Assess the morphology of the red blood cells.
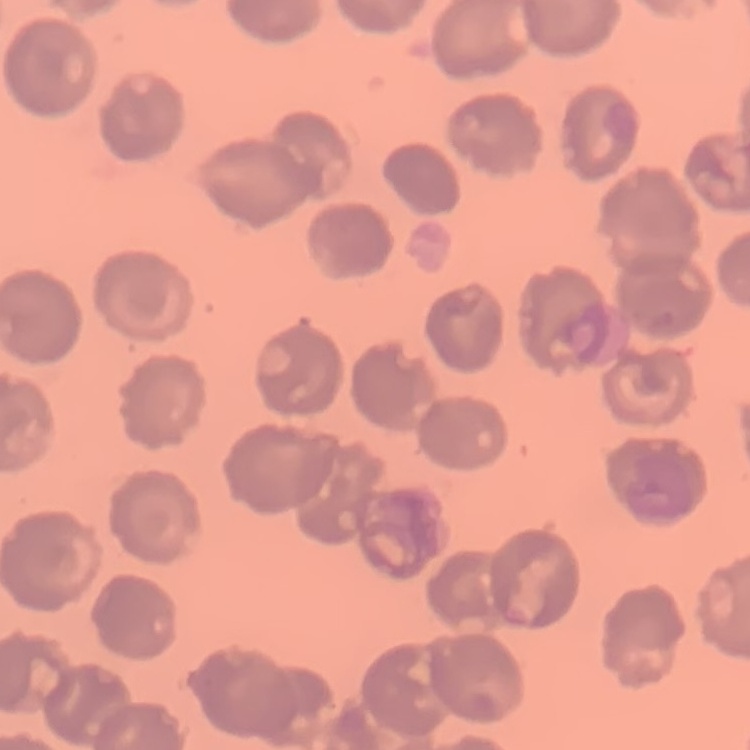
They show no rouleaux formation.

Stained with either Field's or Giemsa. Thin peripheral smear. Square crop of a larger photomicrograph.